Classify this cell by malaria status.
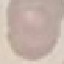
It is uninfected.

Summary:
  - Stain: Giemsa
  - Capture: smartphone camera at the microscope eyepiece
  - Preparation: thin blood film
  - Image type: cell patch, automatically extracted from a larger field of view and resized to 64 × 64 pixels